Name the parasite shown.
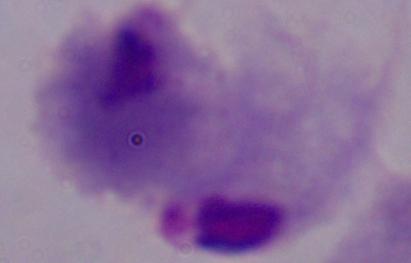
A trichomonad.

Captured at 1000x magnification. Photomicrograph.